State which parasite is depicted.
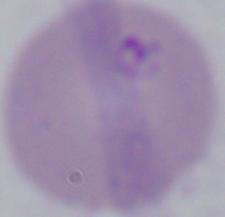

This is Babesia.

Micrograph. Captured at 1000x magnification.